Assess the morphology of the erythrocytes.
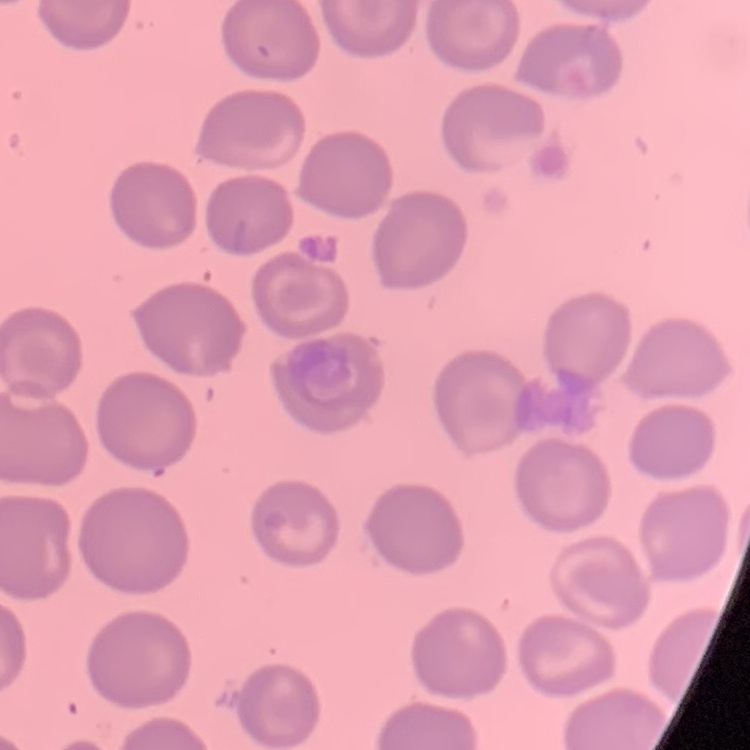
They show no rouleaux formation.

preparation: thin blood smear
image_type: one tile cut from a larger photomicrograph
stain: Field's or Giemsa